Assess for malaria.
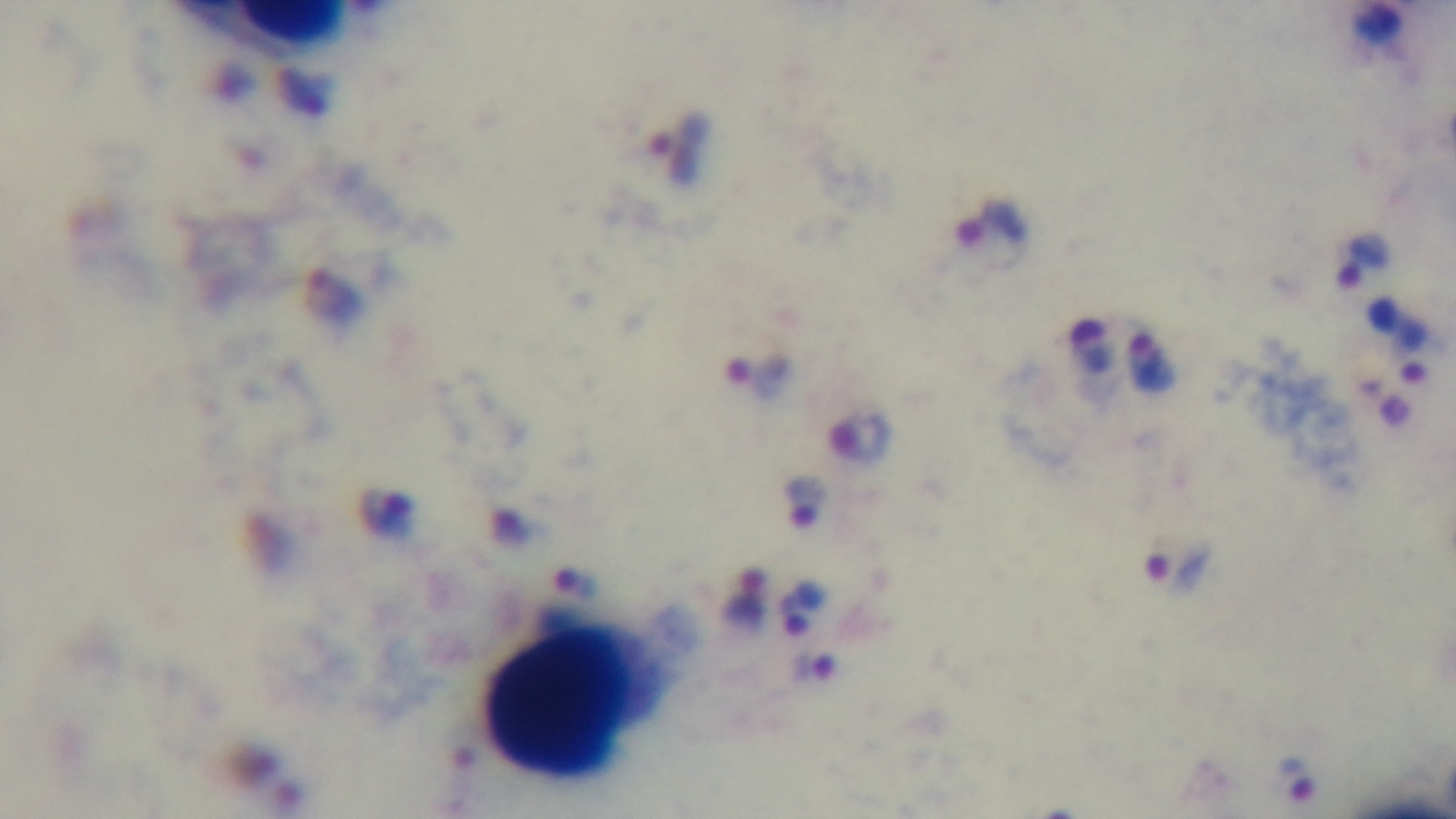
Positive.

field of view = single
stain = Giemsa
objective = 100x oil immersion
modality = light microscopy
capture = mounted 4K digital camera
preparation = thick smear